Report the malaria status of this cell.
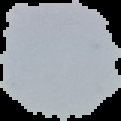

Uninfected.

Cell region segmented out of the field of view; the surrounding area is masked to black. From a thin blood smear. Image is 121×121 pixels.